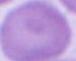

identification = red blood cell
modality = micrograph
magnification = 1000x